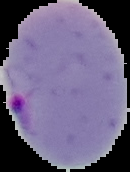
image type = cell region segmented out of the field of view; surrounding area masked to black
image size = 130×172 pixels
preparation = thin blood film
result = Plasmodium parasites identified